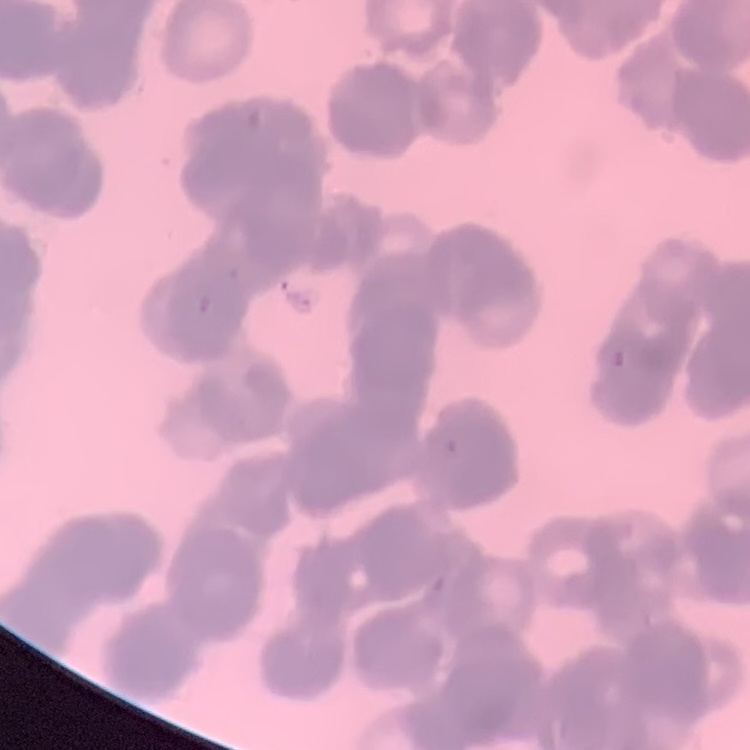

red_blood_cell_morphology: rouleaux formation
image_type: one tile cut from a larger photomicrograph
preparation: thin blood film
stain: Field's or Giemsa